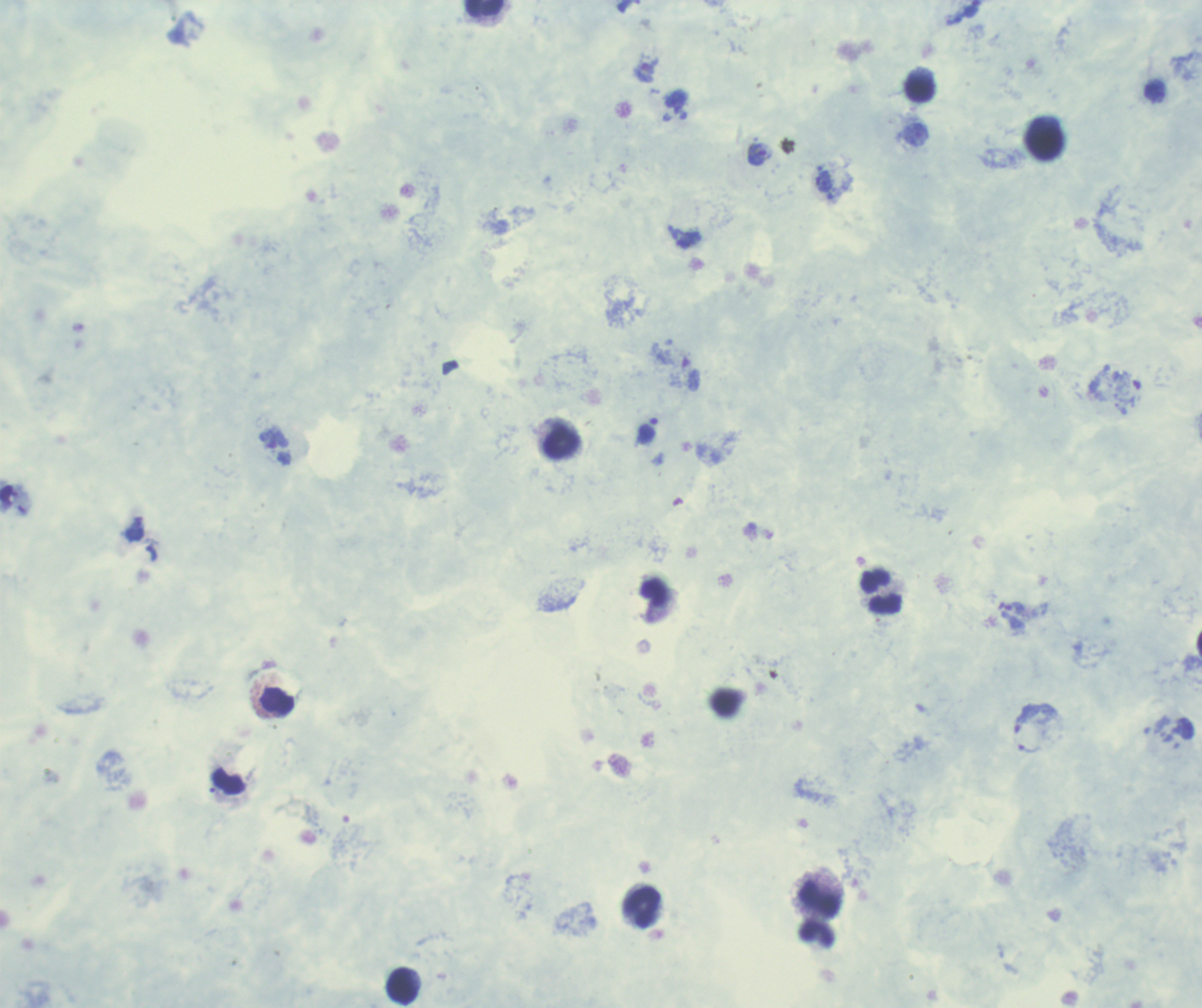

Approximate centers as (x, y) in pixels. Trophozoite locations: (643, 72), (760, 155), (824, 182), (274, 440), (1015, 608). Leukocyte locations: (482, 8), (918, 90), (1044, 143), (562, 442), (880, 591), (276, 701), (818, 899), (640, 907), (816, 934), (402, 986). 100x magnification. Image is 1202×1008 pixels. Result: positive for Plasmodium parasites. Previously used in an actual diagnosis. Romanowsky-stained preparation. Background quality: unsatisfactory. Thick smear of blood. One field from this slide.